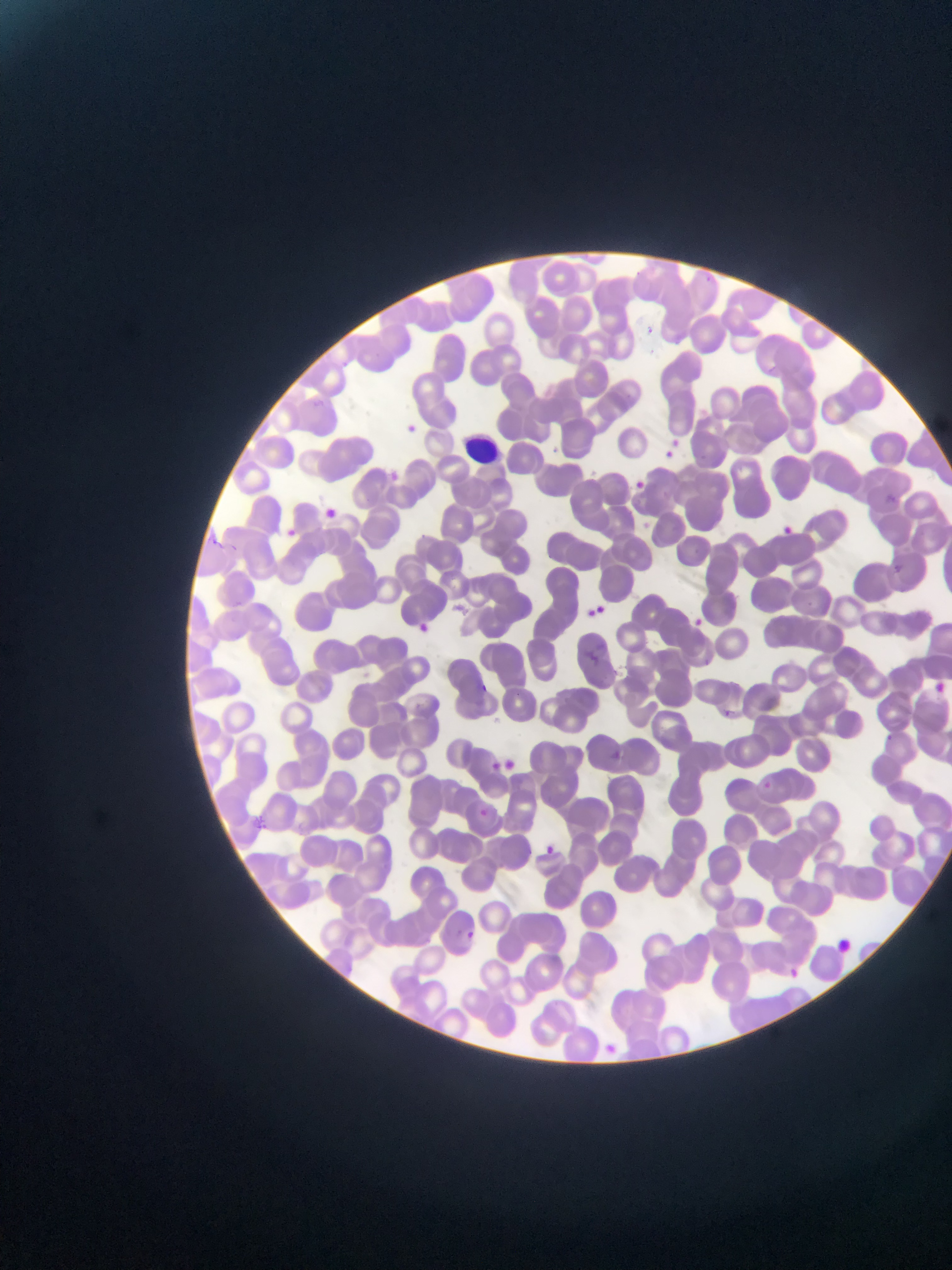
{
  "leukocyte_locations": "approximate bounding boxes as [left, top, right, bottom] in pixels: [456, 416, 521, 475]",
  "capture": "mobile-phone photograph through a microscope",
  "plasmodium_parasite_locations": "approximate bounding boxes as [left, top, right, bottom] in pixels: [642, 312, 669, 338], [405, 408, 430, 440], [657, 428, 697, 462], [633, 475, 654, 497], [321, 490, 333, 522], [779, 511, 801, 540], [283, 520, 308, 542], [582, 599, 619, 619], [690, 609, 712, 626], [418, 621, 445, 635], [932, 674, 952, 700], [477, 679, 504, 695], [602, 748, 647, 765], [492, 759, 521, 776], [476, 796, 495, 821], [531, 834, 568, 854], [782, 957, 816, 988]",
  "image_size": "952×1270 pixels",
  "field_of_view": "single",
  "country": "Ghana",
  "preparation": "thin blood film"
}